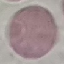
result: no malaria parasites seen
capture: smartphone through the microscope eyepiece
preparation: thin blood smear
image_type: automatically extracted cell patch, resized to 64 × 64 pixels
stain: Giemsa